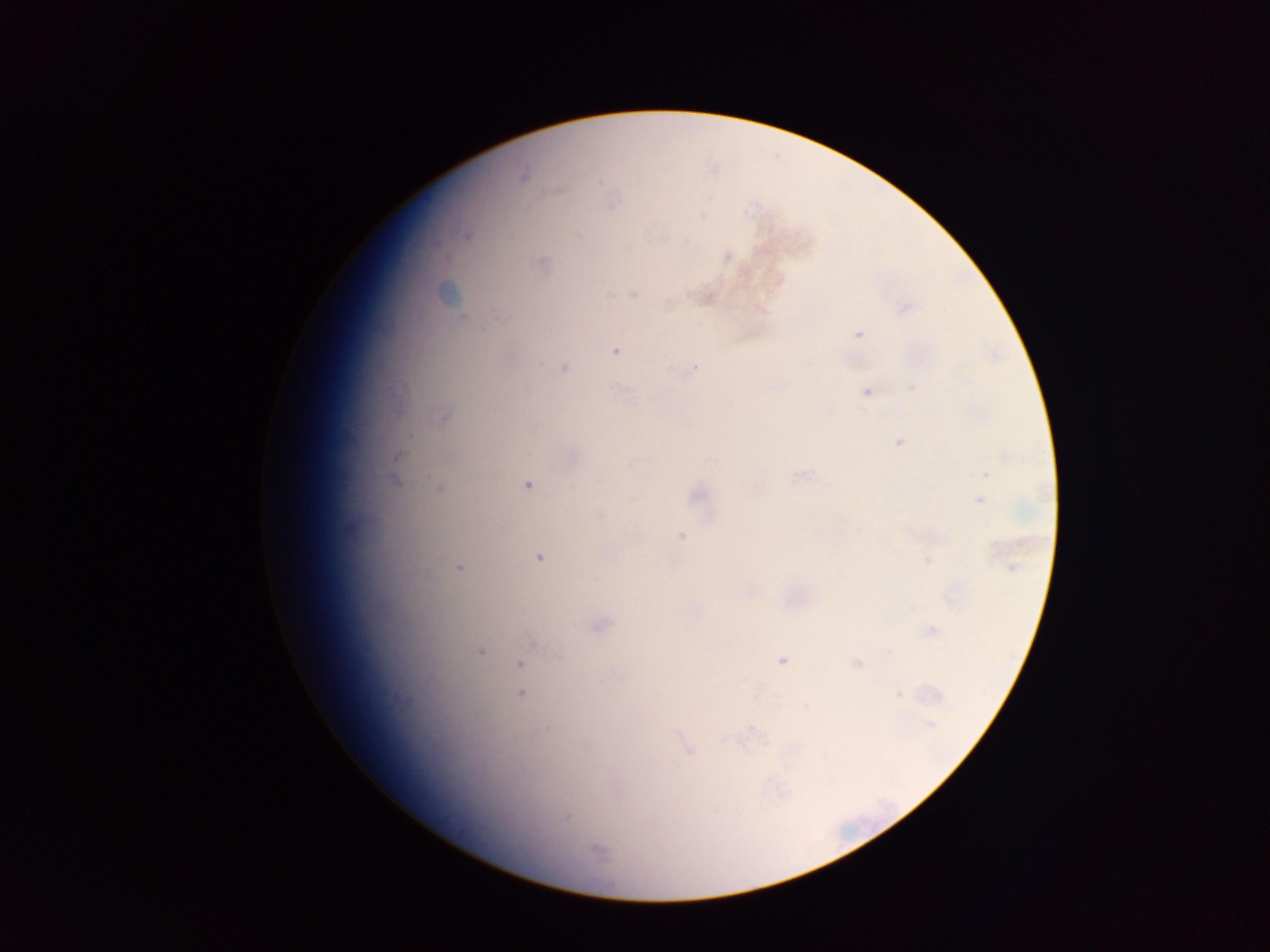

preparation: thick blood film
malaria_parasite_locations: 'approximate centers as {x, y} in pixels: {523, 174}, {557, 191}, {700, 216}, {576, 234}, {728, 256}, {542, 261}, {634, 293}, {609, 295}, {760, 308}, {906, 308}, {859, 334}, {615, 351}, {694, 366}, {564, 367}, {911, 387}, {867, 392}, {900, 442}, {1006, 455}, {397, 456}, {711, 460}, {986, 474}, {801, 476}, {527, 484}, {439, 488}, {758, 490}, {697, 495}, {980, 499}, {599, 515}, {681, 536}, {538, 557}, {928, 561}, {459, 567}, {1013, 567}, {601, 625}, {932, 631}, {534, 645}, {479, 651}, {558, 652}, {782, 660}, {857, 663}, {520, 665}, {520, 693}, {899, 695}, {930, 724}, {547, 729}, {753, 730}, {724, 740}, {688, 750}, {566, 817}, {597, 849}'
country: Ghana
field_of_view: single
capture: mobile-phone photograph through a microscope
image_size: 1270×952 pixels